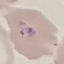

result = malaria parasites identified
capture = smartphone camera at the microscope eyepiece
stain = Giemsa
preparation = thin blood film
image type = cell patch, automatically extracted from a larger field of view and resized to 64 × 64 pixels